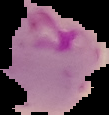
preparation = thin blood film
result = malaria parasites identified
image size = 109×115 pixels
image type = cell region segmented out of the field of view; surrounding area masked to black